State the blood parasite species.
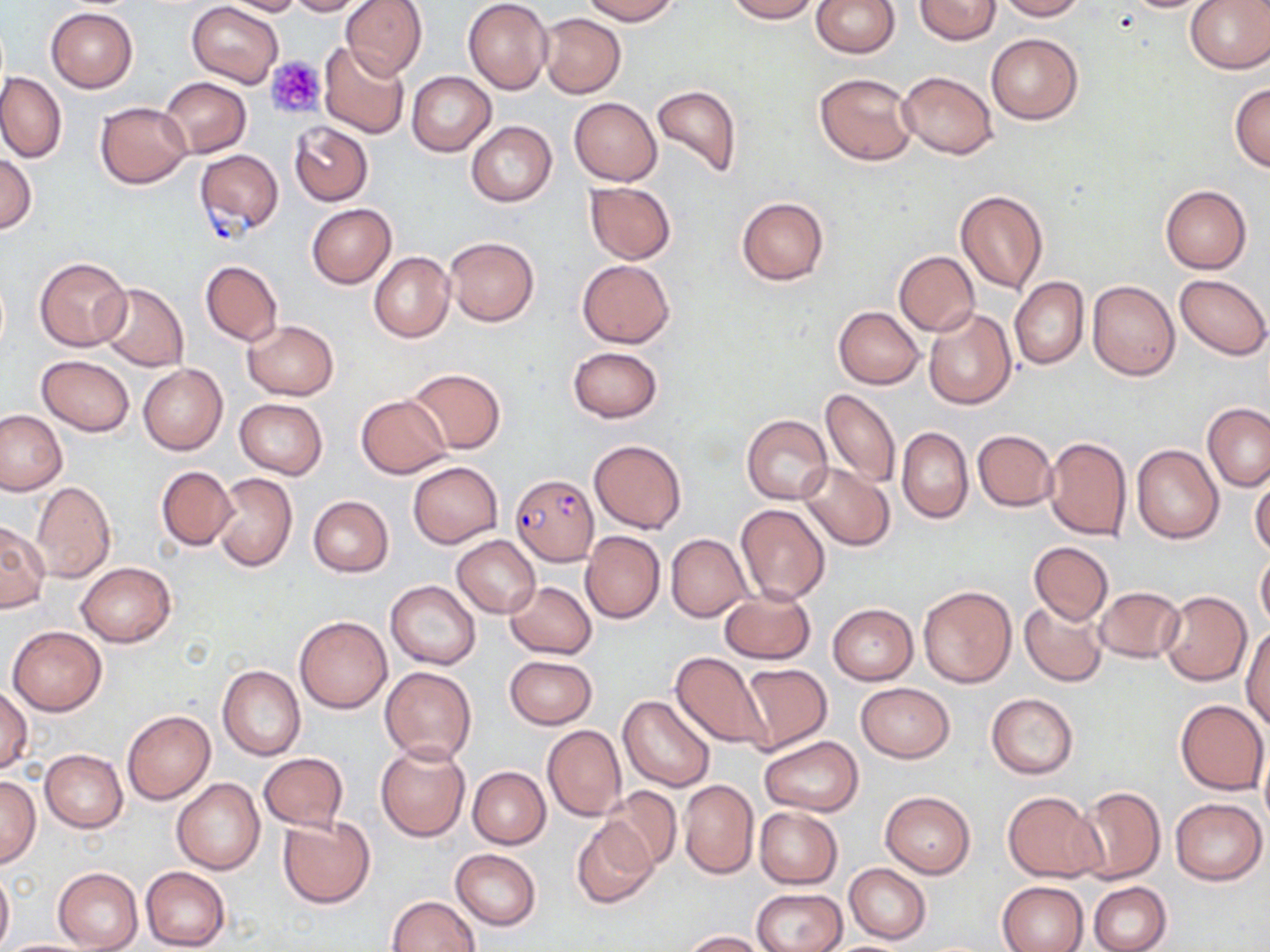
Plasmodium falciparum.

Approximate bounding boxes as [x1, y1, x2, y2] in pixels. Platelet locations: [267, 57, 327, 120]. Uninfected red blood cell locations: [219, 0, 307, 17], [284, 0, 368, 15], [341, 0, 427, 79], [463, 0, 553, 93], [580, 0, 679, 24], [723, 0, 817, 22], [811, 0, 899, 57], [915, 0, 1000, 45], [995, 0, 1087, 20], [1116, 0, 1223, 12], [186, 1, 283, 88], [1185, 1, 1270, 73], [46, 8, 138, 92], [537, 13, 625, 97], [987, 34, 1082, 124], [318, 42, 412, 139], [407, 71, 496, 156], [898, 71, 997, 159], [0, 72, 67, 162], [813, 72, 918, 166], [159, 76, 250, 158], [651, 83, 742, 180], [1230, 83, 1270, 173], [569, 97, 662, 185], [95, 101, 192, 187], [465, 120, 556, 207], [289, 121, 373, 205], [0, 153, 36, 234], [584, 183, 676, 263], [1160, 184, 1252, 274], [955, 190, 1048, 294], [737, 196, 828, 285], [307, 204, 396, 288], [443, 237, 539, 326], [893, 251, 980, 336], [370, 252, 454, 343], [35, 256, 130, 351], [578, 259, 674, 347], [200, 260, 282, 344], [1175, 274, 1270, 359], [1010, 276, 1088, 369], [1088, 280, 1180, 381], [96, 283, 188, 371], [833, 306, 923, 389], [924, 308, 1017, 410], [244, 320, 338, 400], [567, 346, 662, 422], [36, 355, 134, 435], [138, 363, 228, 454], [407, 368, 506, 453], [821, 388, 901, 488], [355, 394, 451, 478], [234, 398, 328, 478], [1203, 402, 1270, 492], [0, 409, 68, 496], [742, 415, 833, 504], [896, 427, 972, 523], [973, 430, 1056, 511], [1043, 436, 1132, 540], [590, 439, 686, 534], [1132, 444, 1224, 544], [408, 461, 502, 548], [799, 463, 894, 550], [155, 466, 236, 550], [210, 472, 298, 572], [1250, 477, 1270, 557], [32, 481, 115, 582], [308, 496, 392, 577], [735, 503, 830, 605], [0, 520, 48, 613], [581, 529, 664, 624], [667, 533, 752, 622], [453, 534, 540, 618], [1028, 541, 1113, 625], [1256, 551, 1270, 631], [76, 563, 176, 646], [386, 581, 480, 669], [506, 581, 596, 658], [919, 584, 1015, 687], [719, 587, 816, 664], [1093, 587, 1185, 663], [1158, 590, 1252, 685], [1019, 599, 1109, 687], [828, 603, 919, 685], [294, 615, 392, 713], [7, 624, 107, 716], [1242, 624, 1270, 731], [671, 653, 770, 750], [504, 655, 597, 729], [739, 662, 832, 753], [218, 665, 305, 761], [380, 666, 477, 764], [856, 682, 955, 762], [0, 686, 32, 774], [986, 692, 1078, 778], [619, 694, 715, 792], [1176, 699, 1268, 794], [122, 711, 214, 803], [542, 725, 626, 821], [760, 736, 863, 816], [375, 742, 470, 842], [40, 749, 127, 832], [259, 753, 348, 830], [468, 766, 550, 848], [0, 775, 42, 867], [171, 779, 265, 875], [679, 780, 759, 879], [602, 786, 683, 873], [1073, 786, 1165, 884], [880, 790, 976, 878], [1003, 791, 1105, 882], [1170, 798, 1266, 885], [754, 807, 842, 888], [277, 816, 375, 909], [572, 819, 657, 908], [451, 848, 541, 929], [844, 864, 931, 942], [53, 867, 142, 952], [140, 867, 231, 951], [0, 869, 13, 949], [996, 881, 1089, 951], [1088, 881, 1171, 952], [753, 888, 847, 952], [387, 895, 480, 952], [682, 930, 766, 951], [0, 939, 95, 952]. Plasmodium falciparum-infected red blood cell locations: [196, 148, 283, 245], [509, 473, 599, 565]. Optical microscopy. Image is 1270×952 pixels. Thin blood film. 1000x magnification. Single field of view. May-Grünwald-Giemsa-stained preparation.